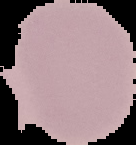
malaria status = uninfected
image type = segmented cell region with the area outside set to black
image size = 136×145 pixels
preparation = thin blood film